Point out each Plasmodium parasite.
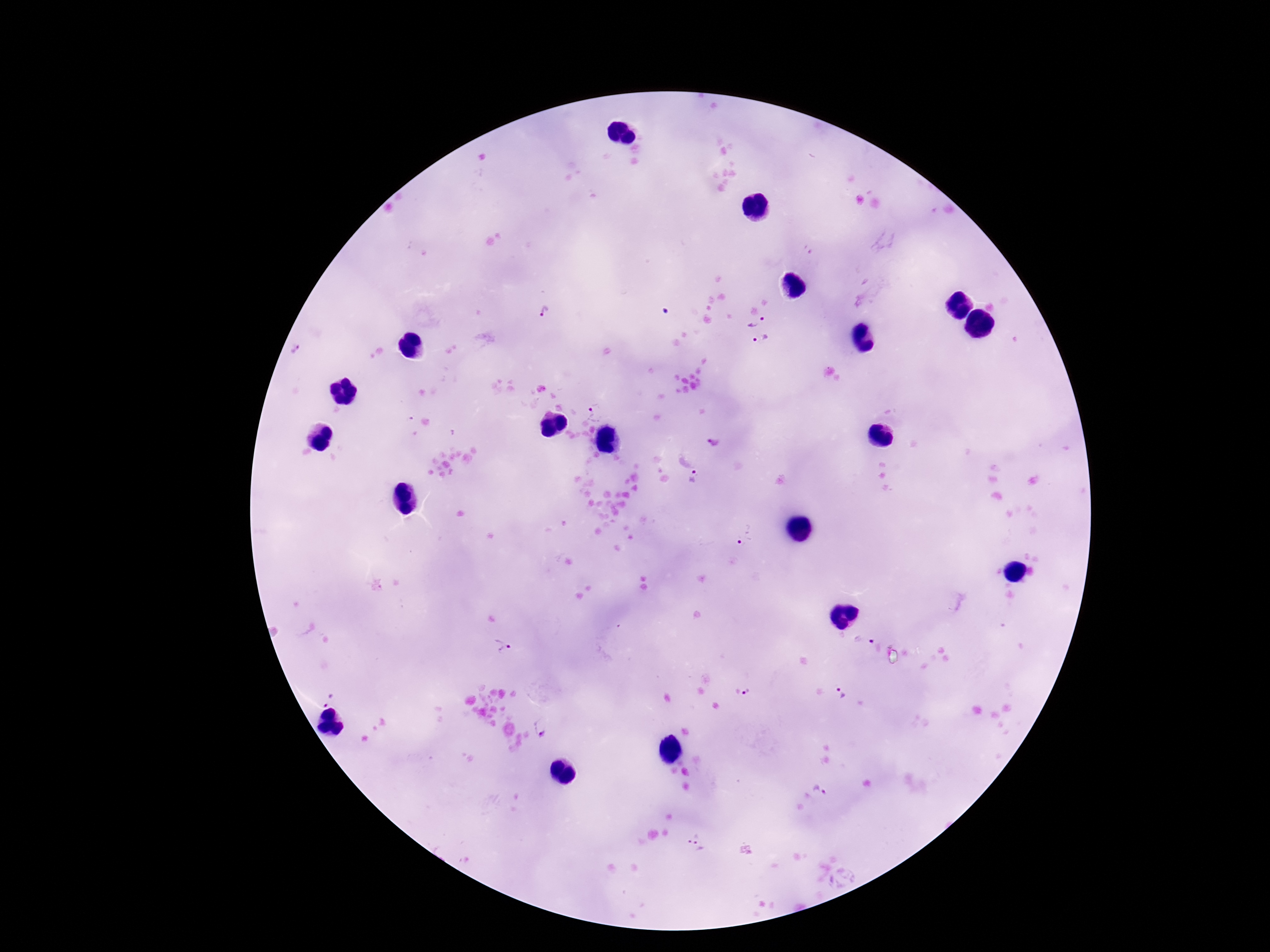

Approximate centers as [x, y] in pixels.
Plasmodium parasites: [544, 312], [757, 320], [762, 339], [297, 352], [596, 413], [715, 444], [696, 477], [743, 534], [863, 639], [502, 646], [841, 692], [747, 693], [327, 699], [542, 728], [820, 787], [696, 841].

Photographed through the microscope eyepiece with a smartphone camera. Image is 1270×952 pixels. 100x magnification. Patient malaria status: infected. Giemsa-stained preparation. Thick peripheral-blood smear. One field from this slide.